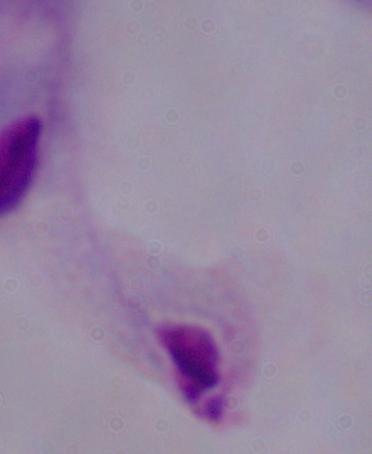

Summary:
  - Modality: micrograph
  - Magnification: 1000x
  - Identification: trichomonad